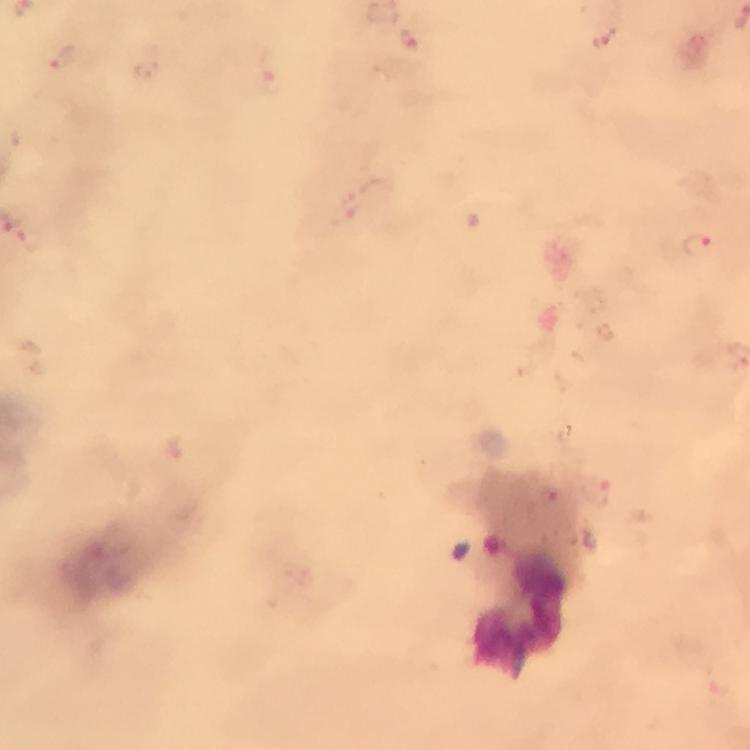
Approximate object centers, in pixels from the top-left corner.
Summary:
  - Plasmodium parasite locations: (x=602, y=37), (x=410, y=39), (x=63, y=56), (x=271, y=83), (x=344, y=209), (x=698, y=245), (x=173, y=449), (x=602, y=492)
  - Leukocyte locations: (x=520, y=615)
  - Preparation: thick blood film
  - Immersion oil: applied
  - Cropped from: a single field of view
  - Context: from a diagnostic examination for malaria
  - Image size: 750×750 pixels
  - Capture: smartphone camera through the microscope
  - Magnification: 100x
  - Stain: Giemsa